Locate every malaria parasite.
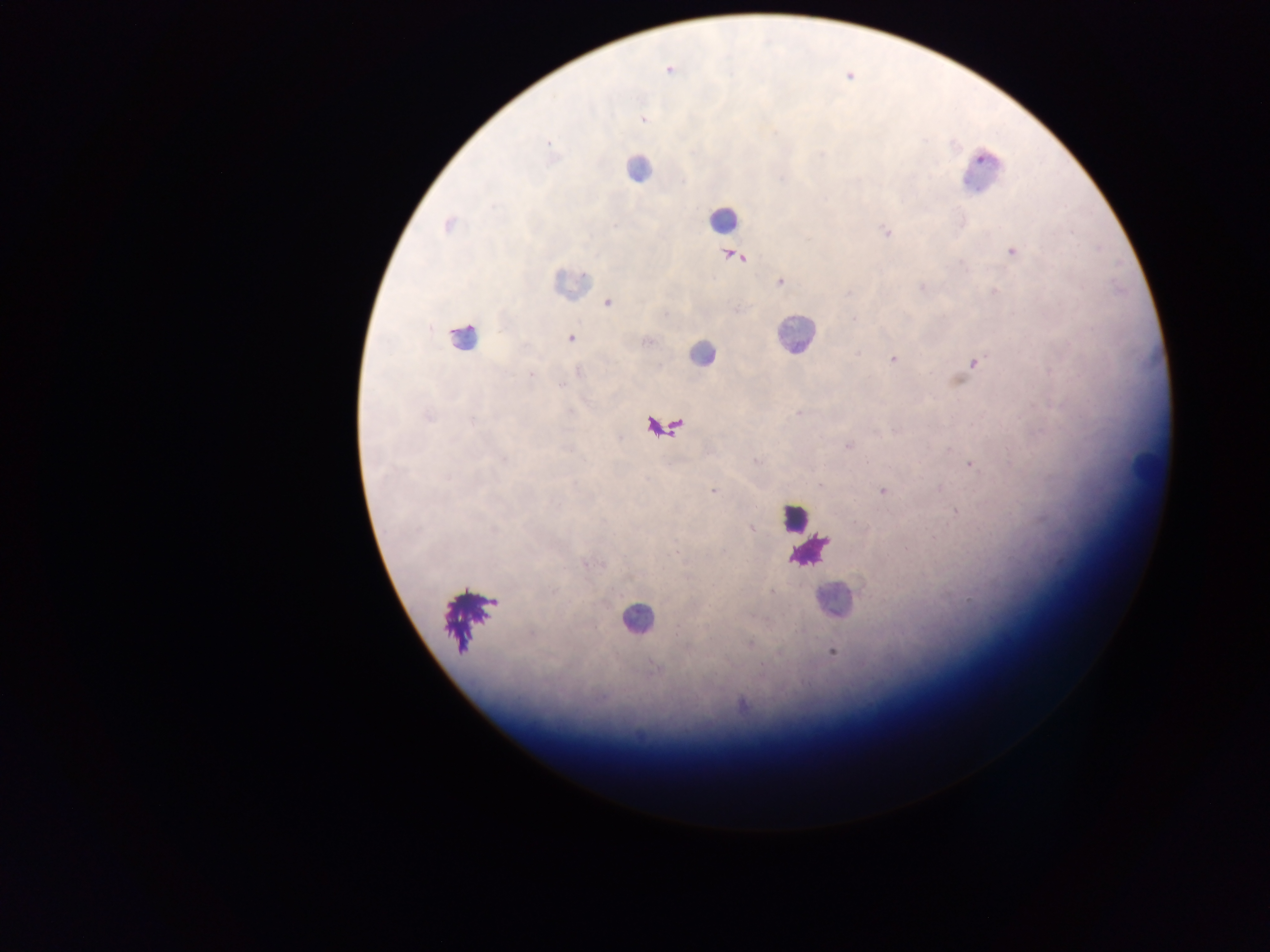

Approximate centers as (x, y) in pixels.
Malaria parasites: (669, 70), (643, 119), (548, 142), (982, 158), (447, 225), (886, 231), (1012, 251), (736, 257), (780, 282), (608, 303), (853, 319), (571, 338), (647, 342), (893, 358), (974, 362), (530, 374), (798, 413), (428, 416), (472, 420), (848, 446), (504, 459), (756, 461), (868, 461), (970, 465), (819, 484), (713, 491), (882, 491), (955, 512), (751, 528), (494, 531), (905, 548), (676, 552), (585, 564), (772, 592), (749, 644), (687, 650), (779, 652), (832, 652), (655, 668), (741, 704).

leukocyte locations = approximate centers as (x, y) in pixels: (638, 169), (723, 219), (570, 282), (795, 334), (461, 336), (701, 353), (1144, 464), (794, 519), (832, 599), (637, 617)
preparation = thick blood smear
field of view = single
capture = mobile-phone photograph through a microscope
country = Ghana
image size = 1270×952 pixels